State which parasite is depicted.
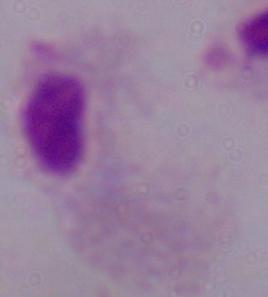
This is a trichomonad.

Captured at 1000x magnification. Micrograph.